Name the parasite shown.
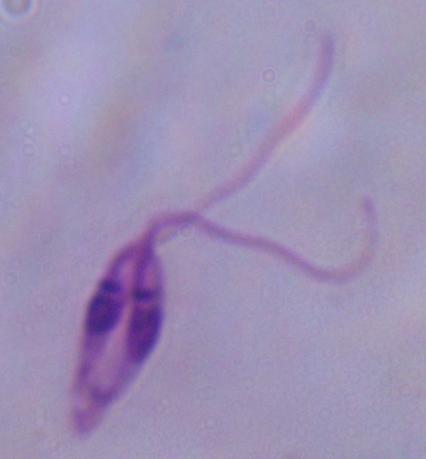
This is Leishmania.

Summary:
  - Modality: micrograph
  - Magnification: 1000x